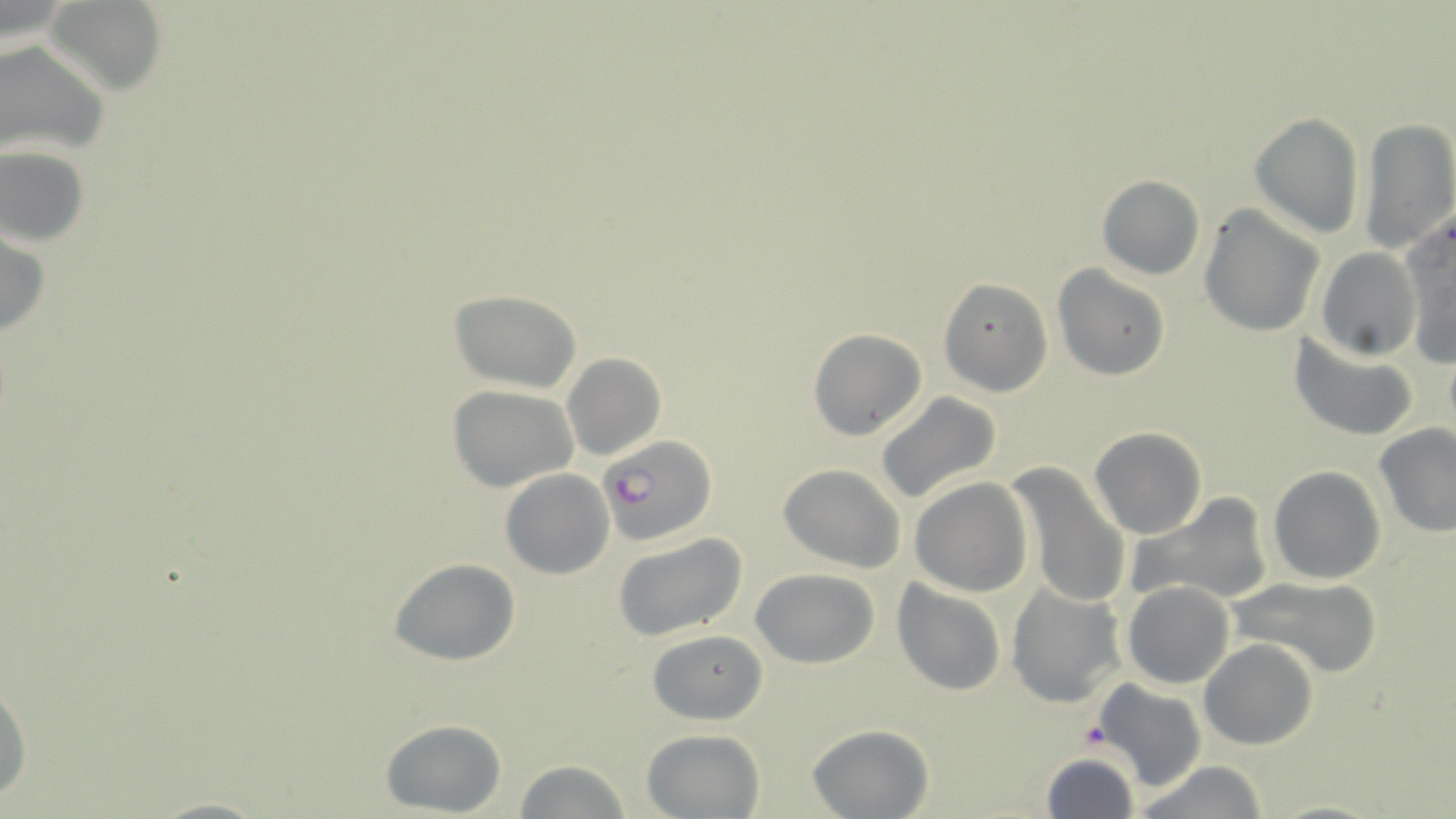

Approximate bounding boxes as (x1, y1, x2, y2) in pixels. Platelet locations: (1076, 722, 1113, 751). Plasmodium falciparum-infected red blood cell locations: (598, 433, 718, 547). Uninfected red blood cell locations: (48, 2, 166, 90), (0, 39, 110, 162), (1248, 111, 1366, 240), (1356, 117, 1456, 255), (0, 145, 91, 248), (1096, 175, 1205, 280), (1198, 206, 1323, 337), (1400, 215, 1456, 367), (0, 228, 51, 342), (1316, 248, 1422, 361), (1052, 266, 1171, 381), (939, 277, 1052, 396), (448, 288, 584, 394), (807, 327, 928, 442), (1290, 332, 1419, 442), (560, 352, 667, 461), (447, 384, 580, 493), (875, 393, 1002, 507), (1374, 423, 1456, 538), (1088, 427, 1207, 538), (1005, 462, 1130, 610), (777, 463, 907, 571), (1268, 466, 1386, 584), (500, 468, 614, 579), (910, 477, 1033, 597), (1127, 492, 1274, 608), (612, 532, 746, 641), (388, 558, 521, 667), (751, 568, 877, 668), (1224, 576, 1386, 680), (891, 578, 1007, 696), (1122, 580, 1234, 689), (1005, 583, 1126, 709), (648, 629, 766, 726), (1199, 640, 1320, 750), (1092, 679, 1207, 790), (0, 682, 32, 807), (378, 718, 507, 815), (806, 724, 934, 818), (640, 727, 766, 818), (1040, 751, 1140, 819), (512, 760, 634, 818), (1130, 762, 1271, 819), (146, 796, 273, 818), (1264, 797, 1389, 819). Slide-level diagnosis: Plasmodium falciparum. May-Grünwald-Giemsa-stained preparation. Optical microscopy. One field of a larger specimen. Image is 1456×819 pixels. Thin blood smear. 1000x magnification.